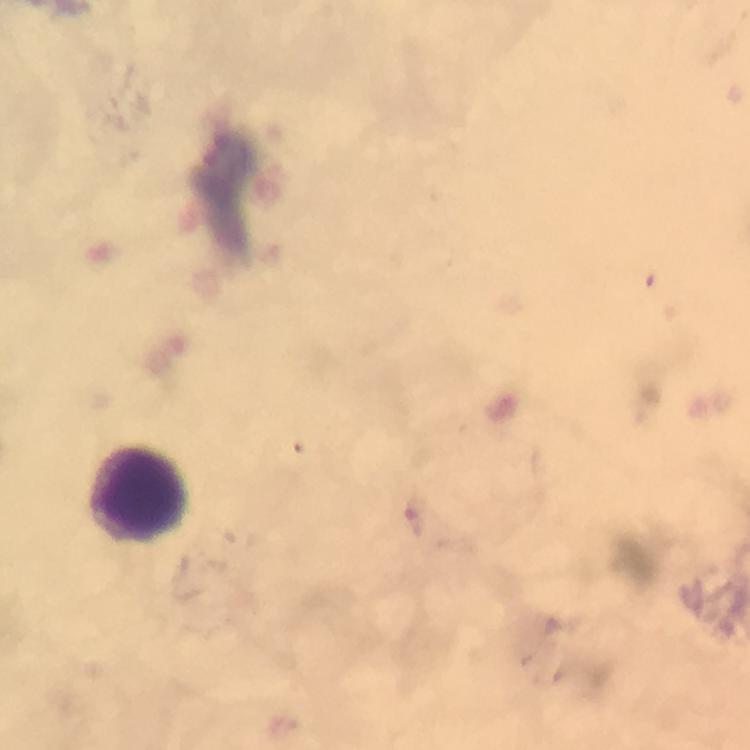 Approximate centers as (x, y) in pixels. Leukocyte locations: (140, 493). Photographed through the microscope with a smartphone camera. 100x magnification. Plasmodium parasites: none detected. From a malaria diagnostic workup. Thick smear. Immersion oil applied. Giemsa-stained preparation. Image is 750×750 pixels. A crop from one field of view.